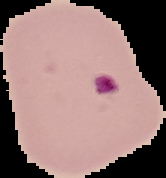

Summary:
  - Preparation: thin blood film
  - Malaria status: parasitized
  - Image size: 166×178 pixels
  - Image type: segmented cell region with the area outside set to black